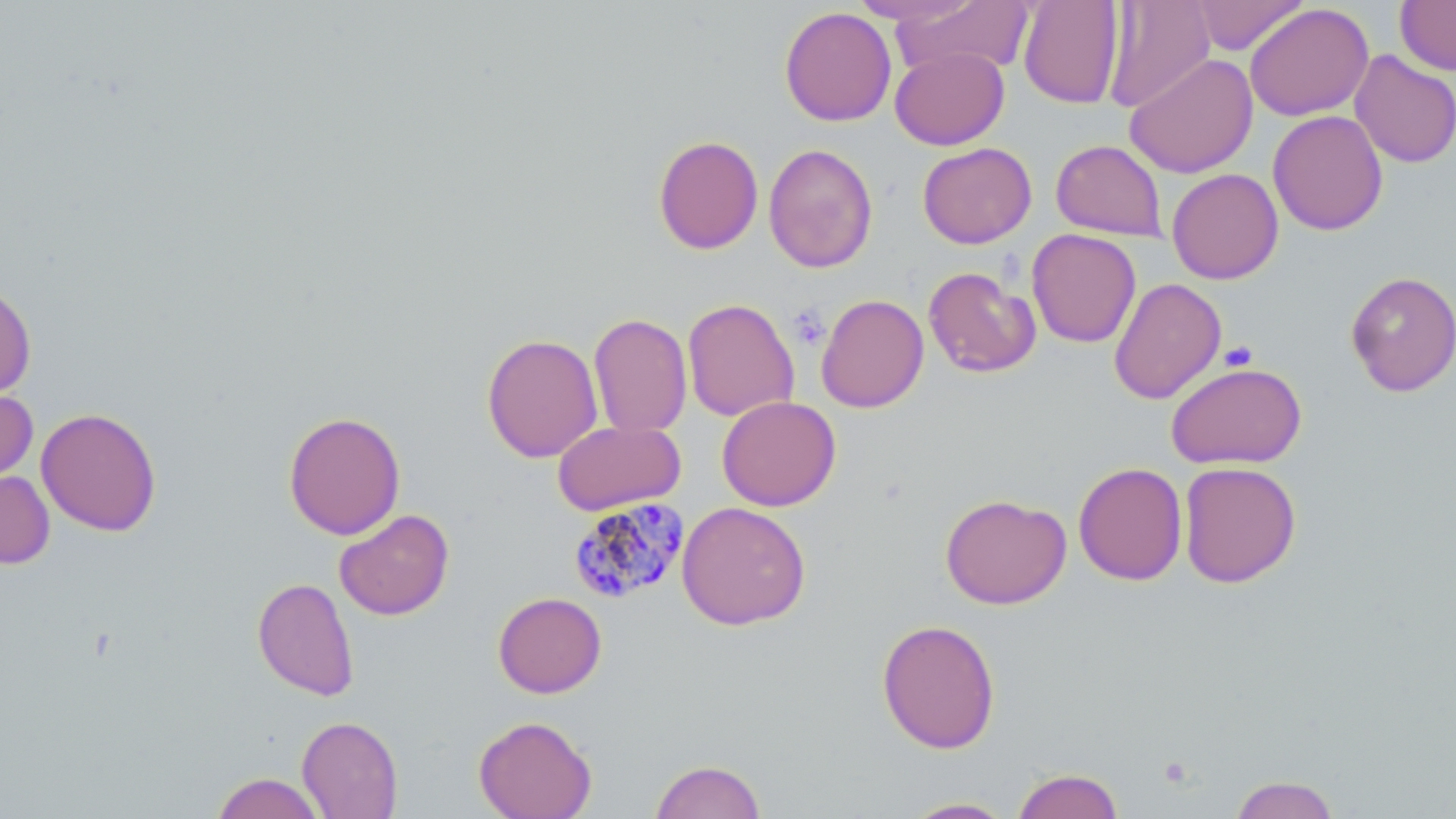
Approximate bounding boxes as named x1/y1/x2/y2 corners in pixels. Platelet locations: (x1=787, y1=305, x2=829, y2=348), (x1=1219, y1=341, x2=1258, y2=372). Uninfected red blood cell locations: (x1=848, y1=0, x2=983, y2=26), (x1=1018, y1=0, x2=1125, y2=109), (x1=1102, y1=0, x2=1216, y2=113), (x1=1188, y1=0, x2=1309, y2=56), (x1=1395, y1=0, x2=1456, y2=75), (x1=894, y1=1, x2=1035, y2=77), (x1=1244, y1=3, x2=1374, y2=122), (x1=779, y1=6, x2=897, y2=127), (x1=890, y1=46, x2=1009, y2=150), (x1=1350, y1=50, x2=1456, y2=168), (x1=1124, y1=53, x2=1258, y2=179), (x1=1267, y1=109, x2=1389, y2=236), (x1=653, y1=135, x2=764, y2=254), (x1=1051, y1=139, x2=1167, y2=241), (x1=917, y1=142, x2=1037, y2=249), (x1=764, y1=143, x2=879, y2=274), (x1=1167, y1=168, x2=1283, y2=284), (x1=1026, y1=229, x2=1141, y2=348), (x1=923, y1=266, x2=1041, y2=378), (x1=1344, y1=270, x2=1456, y2=397), (x1=1108, y1=278, x2=1228, y2=404), (x1=0, y1=280, x2=37, y2=400), (x1=815, y1=294, x2=929, y2=413), (x1=682, y1=297, x2=799, y2=422), (x1=588, y1=312, x2=693, y2=438), (x1=481, y1=333, x2=603, y2=463), (x1=1166, y1=361, x2=1307, y2=469), (x1=0, y1=387, x2=38, y2=486), (x1=716, y1=395, x2=841, y2=512), (x1=36, y1=407, x2=162, y2=536), (x1=283, y1=410, x2=406, y2=540), (x1=552, y1=419, x2=686, y2=515), (x1=1178, y1=461, x2=1302, y2=588), (x1=1073, y1=462, x2=1188, y2=586), (x1=0, y1=469, x2=55, y2=569), (x1=940, y1=493, x2=1071, y2=609), (x1=676, y1=501, x2=811, y2=631), (x1=334, y1=509, x2=455, y2=621), (x1=252, y1=577, x2=360, y2=701), (x1=493, y1=591, x2=607, y2=698), (x1=876, y1=618, x2=1001, y2=754), (x1=297, y1=715, x2=403, y2=818), (x1=473, y1=715, x2=597, y2=818), (x1=649, y1=759, x2=766, y2=819), (x1=1011, y1=768, x2=1125, y2=819), (x1=211, y1=772, x2=326, y2=819), (x1=1228, y1=775, x2=1341, y2=819), (x1=901, y1=797, x2=1017, y2=818). Plasmodium malariae-infected red blood cell locations: (x1=568, y1=498, x2=690, y2=604). Slide-level diagnosis: Plasmodium malariae. May-Grünwald-Giemsa stain. One field of a larger specimen. Image is 1456×819 pixels. 1000x magnification. Optical microscopy. Thin blood smear.